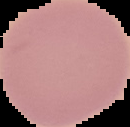

Summary:
  - Image type: segmented cell region with the area outside set to black
  - Result: no malaria parasites seen
  - Image size: 130×127 pixels
  - Preparation: thin blood smear